Give the preparation type.
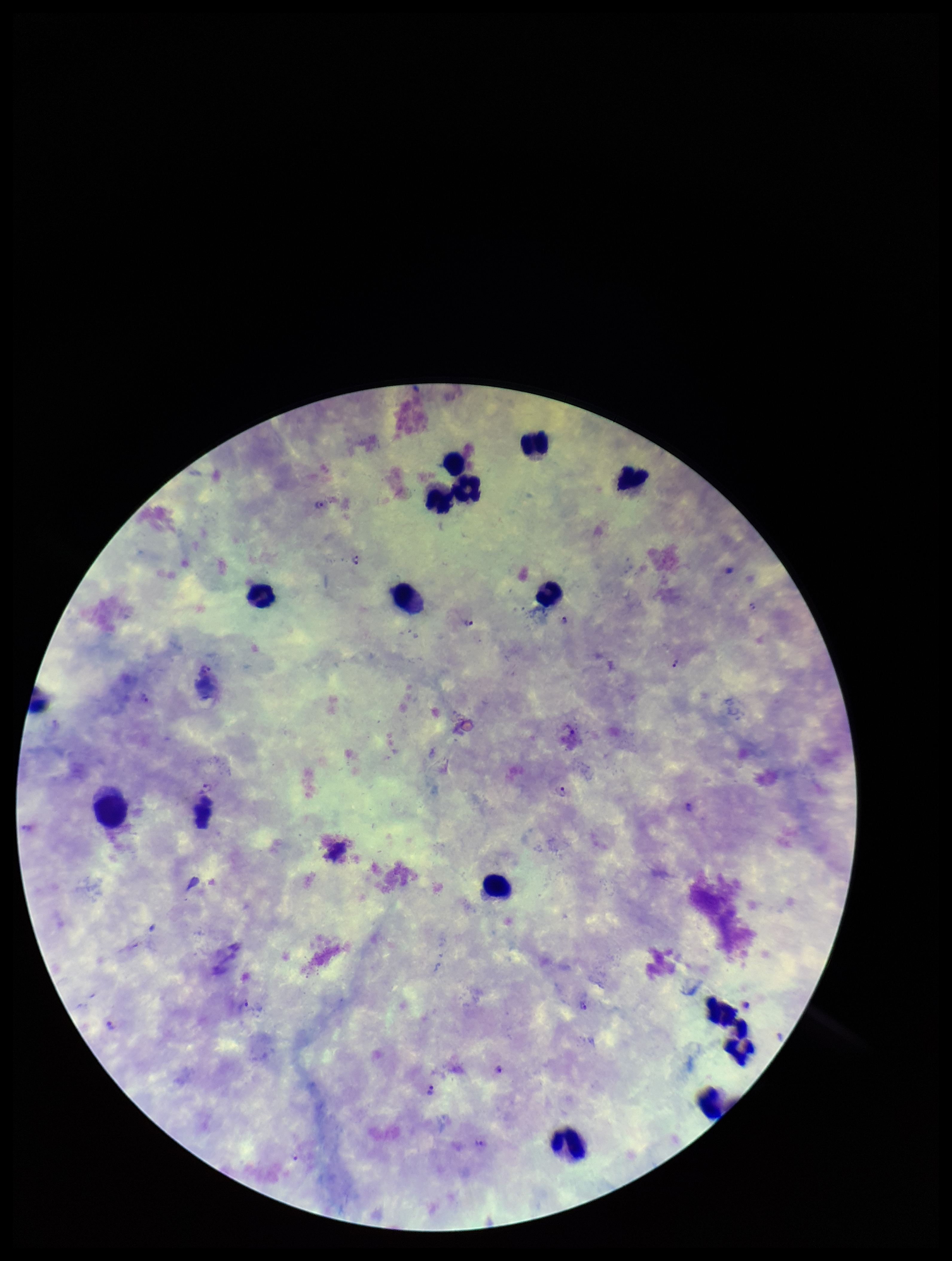
It is a thick blood smear.

Summary:
  - Image size: 952×1261 pixels
  - Patient malaria status: infected
  - Leukocyte count: 15
  - Plasmodium parasites: detected
  - Species reported for this patient: Plasmodium vivax
  - Parasite count: 12
  - Capture: smartphone photograph through the microscope eyepiece
  - Field of view: single
  - Stain: Giemsa